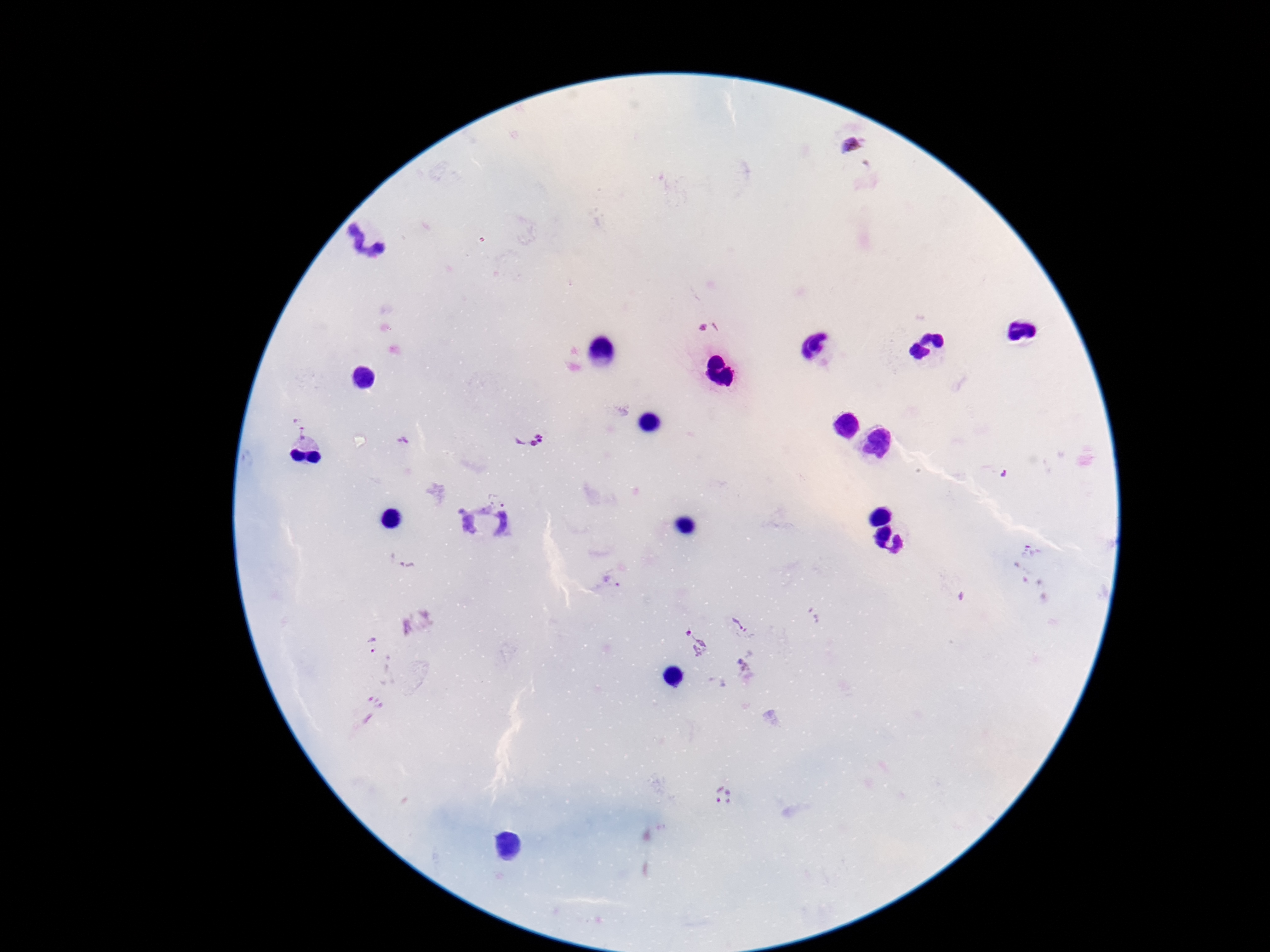

Approximate object centers, in pixels from the top-left corner.
Summary:
  - Plasmodium parasite locations: (x=854, y=145), (x=294, y=419), (x=529, y=438), (x=406, y=440), (x=1004, y=476), (x=501, y=491), (x=486, y=530), (x=1033, y=550), (x=612, y=581), (x=742, y=624), (x=694, y=641), (x=371, y=647), (x=722, y=795)
  - Patient malaria status: infected
  - Magnification: 100x
  - Image size: 1270×952 pixels
  - Stain: Giemsa
  - Preparation: thick peripheral-blood smear
  - Capture: smartphone camera through the microscope eyepiece
  - Field of view: single